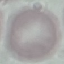
Summary:
  - Result: no malaria parasites detected
  - Stain: Giemsa
  - Capture: smartphone camera at the microscope eyepiece
  - Preparation: thin smear
  - Image type: automatically extracted cell patch, resized to 64 × 64 pixels